Assess the morphology of the red blood cells.
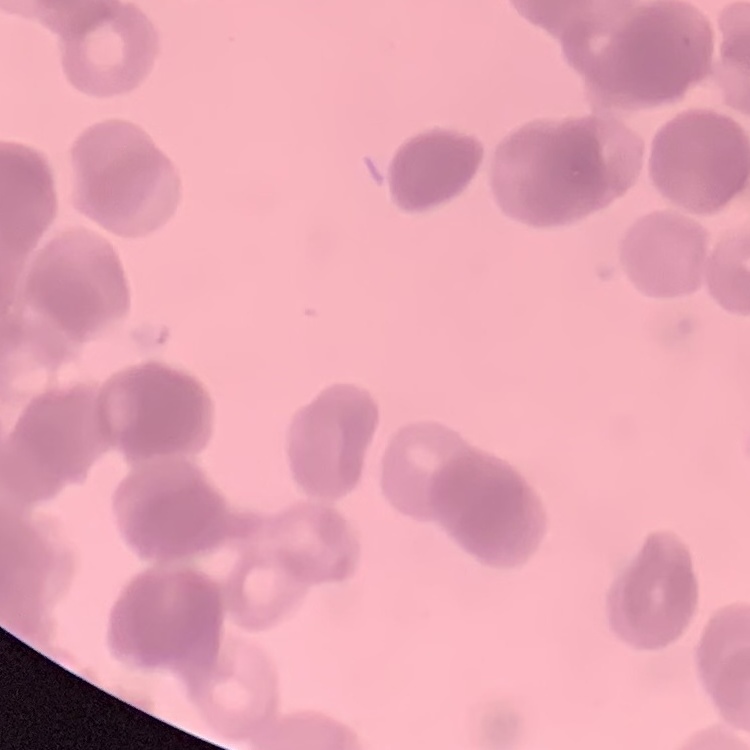

They show rouleaux formation.

Square crop of a larger photomicrograph. Thin peripheral smear. Stained with either Field's or Giemsa.